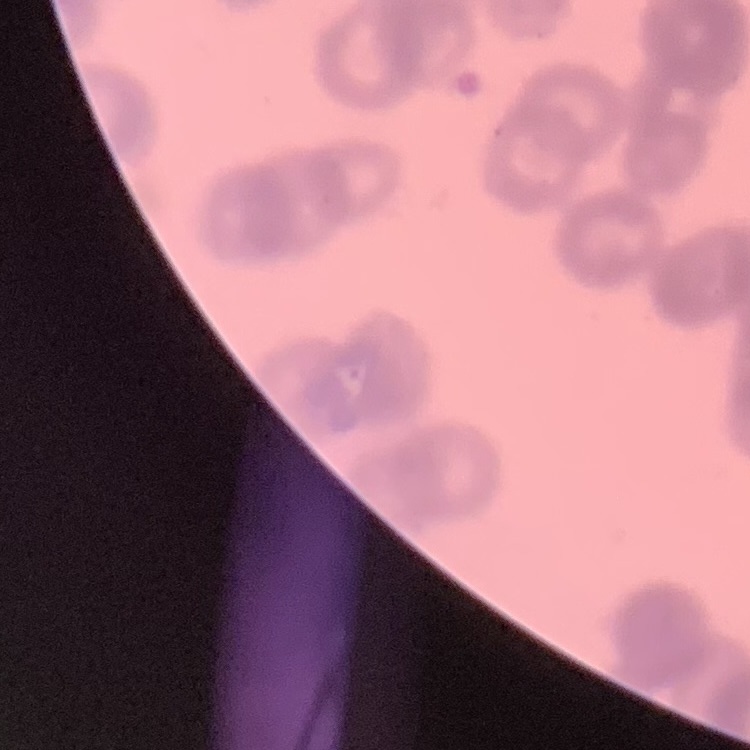 The red blood cells exhibit rouleaux formation. Thin blood film. Field's or Giemsa stain. One tile cut from a larger photomicrograph.